Assess this cell for malaria.
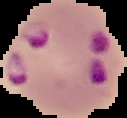
It is parasitized.

Summary:
  - Image type: segmented cell region on a black background
  - Image size: 127×118 pixels
  - Preparation: thin blood smear